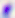
magnification = 400x
identification = Toxoplasma gondii
modality = micrograph